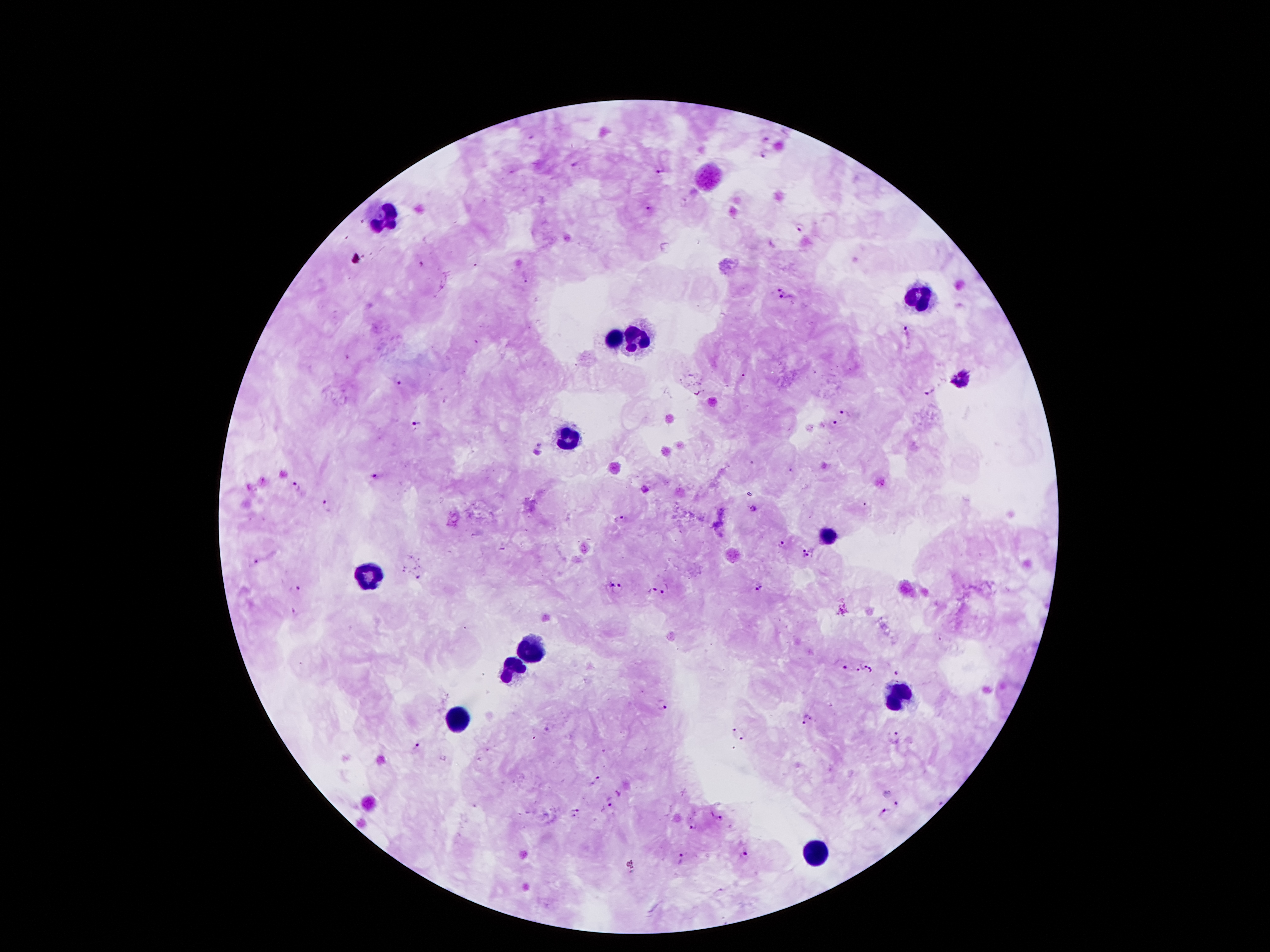

Approximate centers as {x, y} in pixels. Malaria parasite locations: {769, 137}, {765, 156}, {574, 161}, {660, 169}, {648, 208}, {800, 230}, {783, 286}, {784, 297}, {906, 332}, {402, 384}, {931, 391}, {843, 412}, {416, 421}, {834, 421}, {542, 449}, {375, 475}, {296, 484}, {329, 503}, {753, 508}, {621, 517}, {780, 543}, {803, 548}, {806, 555}, {256, 561}, {419, 574}, {608, 585}, {759, 586}, {297, 587}, {618, 590}, {652, 591}, {665, 591}, {294, 610}, {863, 665}, {846, 668}, {857, 669}, {871, 670}, {896, 673}, {664, 706}, {808, 719}, {547, 728}, {733, 732}, {744, 737}, {899, 738}, {416, 746}, {596, 780}, {611, 800}, {896, 802}, {942, 802}, {576, 806}, {886, 811}, {573, 816}, {720, 818}, {693, 826}, {744, 853}, {682, 857}. Leukocyte locations: {708, 177}, {389, 219}, {922, 298}, {637, 338}, {612, 340}, {962, 382}, {568, 441}, {828, 538}, {366, 576}, {524, 647}, {511, 666}, {899, 691}, {456, 718}, {818, 853}. Patient malaria status: positive for Plasmodium falciparum. Giemsa stain. Image is 1270×952 pixels. 100x magnification. One field from this slide. Thick blood smear. Photographed through the microscope eyepiece with a smartphone camera.